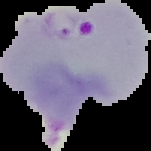

Cell region segmented out of the field of view; the surrounding area is masked to black. Result: malaria parasites identified. Image is 151×151 pixels. From a thin blood film.